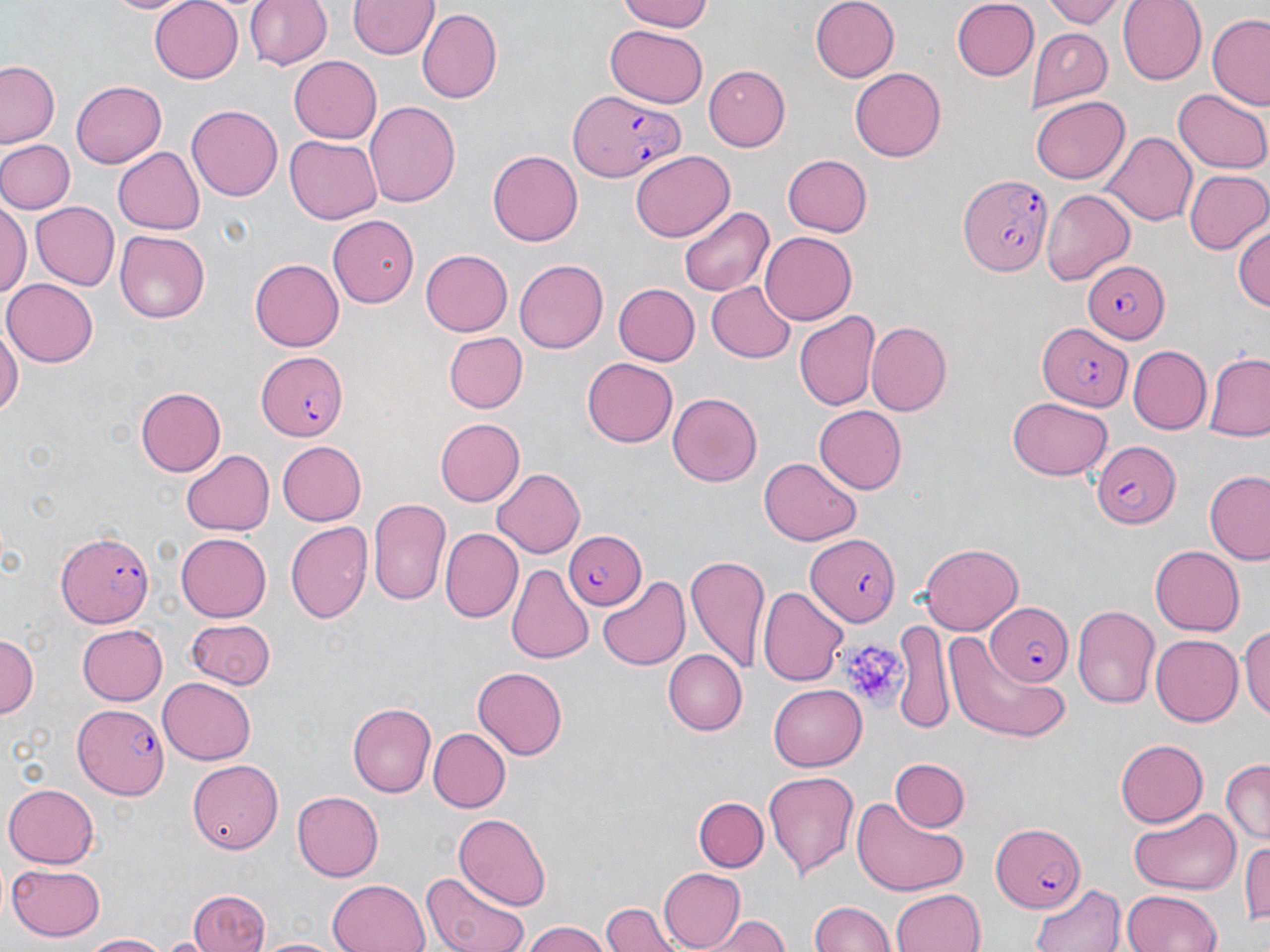
{
  "slide_level_diagnosis": "Plasmodium falciparum",
  "image_size": "1270×952 pixels",
  "magnification": "1000x",
  "platelet_locations": "approximate bounding boxes as named x1/y1/x2/y2 corners in pixels: (x1=838, y1=633, x2=905, y2=713)",
  "field_of_view": "single",
  "stain": "May-Grünwald-Giemsa",
  "uninfected_red_blood_cell_locations": "approximate bounding boxes as named x1/y1/x2/y2 corners in pixels: (x1=104, y1=0, x2=195, y2=16), (x1=148, y1=0, x2=245, y2=83), (x1=247, y1=0, x2=332, y2=72), (x1=614, y1=0, x2=716, y2=32), (x1=808, y1=0, x2=899, y2=83), (x1=950, y1=0, x2=1036, y2=79), (x1=1043, y1=0, x2=1127, y2=26), (x1=1120, y1=0, x2=1205, y2=84), (x1=350, y1=1, x2=438, y2=60), (x1=418, y1=9, x2=502, y2=104), (x1=1208, y1=15, x2=1270, y2=107), (x1=605, y1=25, x2=709, y2=108), (x1=1030, y1=29, x2=1111, y2=108), (x1=290, y1=56, x2=382, y2=143), (x1=1, y1=60, x2=62, y2=148), (x1=703, y1=65, x2=791, y2=150), (x1=850, y1=68, x2=946, y2=161), (x1=71, y1=79, x2=166, y2=166), (x1=1173, y1=86, x2=1270, y2=173), (x1=1031, y1=95, x2=1131, y2=184), (x1=364, y1=102, x2=461, y2=209), (x1=186, y1=105, x2=281, y2=202), (x1=1103, y1=131, x2=1195, y2=227), (x1=286, y1=133, x2=384, y2=224), (x1=0, y1=138, x2=74, y2=214), (x1=111, y1=147, x2=205, y2=235), (x1=629, y1=150, x2=736, y2=240), (x1=487, y1=151, x2=583, y2=246), (x1=783, y1=154, x2=872, y2=237), (x1=1183, y1=169, x2=1270, y2=255), (x1=1040, y1=185, x2=1134, y2=284), (x1=1, y1=198, x2=29, y2=297), (x1=29, y1=202, x2=118, y2=290), (x1=677, y1=204, x2=775, y2=298), (x1=327, y1=214, x2=419, y2=309), (x1=1233, y1=219, x2=1269, y2=313), (x1=114, y1=230, x2=209, y2=322), (x1=757, y1=231, x2=855, y2=325), (x1=421, y1=250, x2=512, y2=336), (x1=514, y1=257, x2=610, y2=353), (x1=249, y1=258, x2=344, y2=352), (x1=4, y1=278, x2=98, y2=365), (x1=708, y1=281, x2=798, y2=361), (x1=613, y1=283, x2=700, y2=366), (x1=794, y1=311, x2=879, y2=412), (x1=0, y1=318, x2=21, y2=424), (x1=866, y1=322, x2=951, y2=417), (x1=443, y1=331, x2=526, y2=411), (x1=1128, y1=345, x2=1212, y2=432), (x1=1204, y1=354, x2=1270, y2=440), (x1=581, y1=358, x2=678, y2=448), (x1=136, y1=387, x2=226, y2=476), (x1=667, y1=391, x2=764, y2=486), (x1=1009, y1=396, x2=1112, y2=479), (x1=815, y1=405, x2=907, y2=494), (x1=435, y1=418, x2=525, y2=505), (x1=277, y1=440, x2=367, y2=525), (x1=182, y1=448, x2=274, y2=536), (x1=759, y1=455, x2=861, y2=544), (x1=492, y1=467, x2=588, y2=558), (x1=1204, y1=470, x2=1270, y2=564), (x1=368, y1=497, x2=451, y2=608), (x1=285, y1=521, x2=373, y2=624), (x1=439, y1=530, x2=522, y2=622), (x1=175, y1=532, x2=270, y2=622), (x1=920, y1=544, x2=1026, y2=633), (x1=1150, y1=545, x2=1246, y2=635), (x1=686, y1=553, x2=771, y2=673), (x1=505, y1=563, x2=593, y2=666), (x1=597, y1=576, x2=691, y2=673), (x1=760, y1=586, x2=848, y2=683), (x1=1072, y1=604, x2=1160, y2=708), (x1=182, y1=616, x2=276, y2=691), (x1=893, y1=618, x2=951, y2=734), (x1=1241, y1=621, x2=1270, y2=725), (x1=75, y1=623, x2=167, y2=705), (x1=1151, y1=632, x2=1243, y2=724), (x1=0, y1=633, x2=38, y2=722), (x1=946, y1=633, x2=1066, y2=740), (x1=662, y1=649, x2=747, y2=734), (x1=472, y1=668, x2=565, y2=759), (x1=158, y1=676, x2=255, y2=764), (x1=769, y1=682, x2=866, y2=767), (x1=347, y1=701, x2=435, y2=798), (x1=427, y1=726, x2=510, y2=812), (x1=1115, y1=739, x2=1210, y2=827), (x1=888, y1=758, x2=968, y2=833), (x1=184, y1=759, x2=281, y2=853), (x1=1221, y1=760, x2=1270, y2=845), (x1=763, y1=770, x2=860, y2=879), (x1=3, y1=784, x2=101, y2=868), (x1=292, y1=791, x2=384, y2=880), (x1=695, y1=795, x2=767, y2=871), (x1=850, y1=796, x2=970, y2=897), (x1=1126, y1=805, x2=1239, y2=893), (x1=454, y1=811, x2=551, y2=908), (x1=1244, y1=837, x2=1270, y2=928), (x1=7, y1=863, x2=105, y2=940), (x1=658, y1=868, x2=746, y2=948), (x1=418, y1=872, x2=531, y2=952), (x1=327, y1=879, x2=431, y2=952), (x1=1027, y1=881, x2=1125, y2=952), (x1=891, y1=888, x2=987, y2=952), (x1=186, y1=890, x2=272, y2=952), (x1=1124, y1=890, x2=1222, y2=952), (x1=809, y1=899, x2=894, y2=952), (x1=601, y1=902, x2=679, y2=952), (x1=708, y1=914, x2=789, y2=952), (x1=520, y1=924, x2=613, y2=952), (x1=79, y1=932, x2=173, y2=951), (x1=255, y1=936, x2=343, y2=952)",
  "preparation": "thin blood smear",
  "plasmodium_falciparum_infected_red_blood_cell_locations": "approximate bounding boxes as named x1/y1/x2/y2 corners in pixels: (x1=570, y1=93, x2=680, y2=185), (x1=961, y1=172, x2=1053, y2=277), (x1=1080, y1=258, x2=1167, y2=343), (x1=1036, y1=321, x2=1133, y2=413), (x1=256, y1=353, x2=348, y2=441), (x1=1089, y1=441, x2=1181, y2=529), (x1=55, y1=528, x2=155, y2=628), (x1=563, y1=528, x2=646, y2=611), (x1=805, y1=534, x2=903, y2=624), (x1=983, y1=602, x2=1071, y2=686), (x1=74, y1=702, x2=171, y2=800), (x1=990, y1=822, x2=1086, y2=915)",
  "modality": "light microscopy"
}